State the blood parasite species.
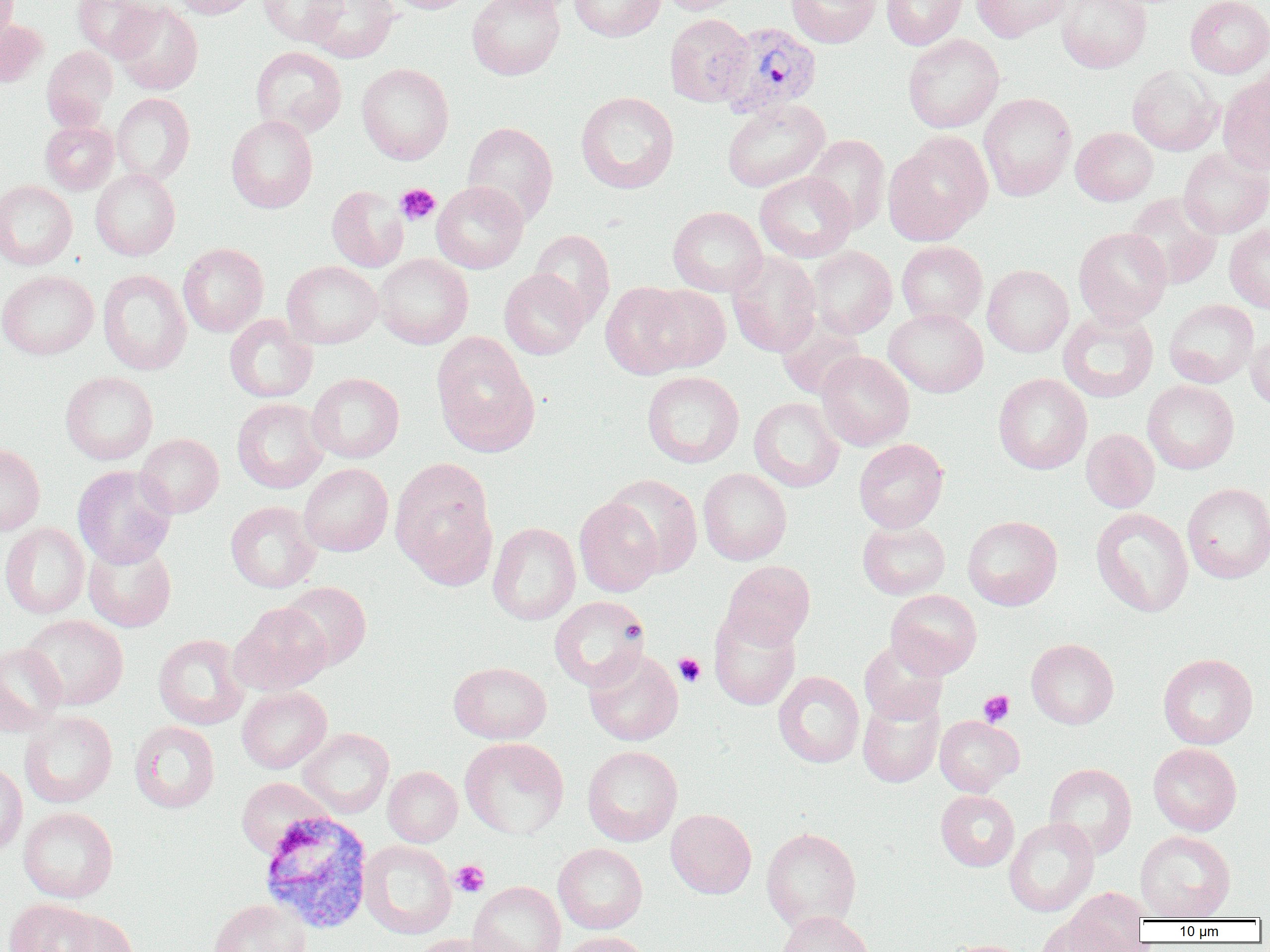

Plasmodium vivax.

Approximate bounding boxes as (x1,y1)-(x2,y2) corner pairs in pixels. Uninfected red blood cell locations: (0,0)-(19,50), (72,0)-(161,60), (168,0)-(258,18), (257,0)-(347,46), (305,0)-(399,62), (386,0)-(478,14), (467,0)-(565,80), (569,0)-(665,41), (659,0)-(747,14), (785,0)-(881,48), (881,0)-(967,50), (886,0)-(977,108), (971,0)-(1070,42), (1056,0)-(1151,73), (1185,0)-(1270,78), (112,1)-(203,95), (664,14)-(754,107), (0,19)-(47,86), (903,33)-(1004,133), (41,46)-(117,131), (250,46)-(347,138), (356,62)-(454,164), (1127,65)-(1221,155), (1218,74)-(1270,175), (576,91)-(679,194), (112,93)-(195,184), (978,93)-(1076,201), (722,98)-(830,192), (226,115)-(318,213), (40,120)-(118,194), (462,121)-(559,226), (1071,127)-(1158,205), (883,132)-(992,246), (804,134)-(890,233), (1178,148)-(1270,238), (91,169)-(180,260), (755,171)-(856,262), (0,181)-(77,270), (431,181)-(529,273), (327,185)-(408,272), (1124,193)-(1223,290), (668,206)-(767,296), (1225,224)-(1270,313), (1073,227)-(1172,327), (529,229)-(615,326), (897,241)-(987,327), (178,243)-(268,336), (807,246)-(897,338), (727,252)-(822,357), (374,254)-(473,349), (282,261)-(383,348), (982,265)-(1074,357), (98,268)-(191,375), (499,268)-(588,359), (0,270)-(98,359), (601,282)-(696,379), (643,284)-(731,373), (1163,299)-(1259,388), (884,308)-(988,397), (1058,309)-(1158,403), (224,314)-(317,403), (776,316)-(866,400), (1246,331)-(1270,411), (432,335)-(540,457), (815,351)-(915,450), (60,371)-(158,465), (642,371)-(744,468), (307,372)-(405,463), (993,373)-(1092,474), (1143,380)-(1239,474), (749,397)-(844,492), (232,398)-(328,493), (1081,428)-(1159,513), (135,433)-(224,518), (854,439)-(948,532), (0,443)-(45,536), (390,458)-(497,584), (298,463)-(393,556), (73,465)-(176,568), (698,468)-(792,565), (605,474)-(703,578), (1182,483)-(1270,583), (574,496)-(664,597), (225,501)-(320,593), (1091,507)-(1194,617), (962,515)-(1062,610), (857,520)-(950,599), (488,522)-(580,625), (0,523)-(89,618), (83,540)-(177,632), (721,560)-(816,648), (279,581)-(371,671), (886,589)-(982,679), (549,596)-(650,691), (229,602)-(332,695), (709,608)-(801,710), (21,614)-(129,710), (153,634)-(249,730), (1026,638)-(1118,729), (859,639)-(948,724), (0,642)-(66,736), (584,649)-(683,746), (1158,653)-(1258,749), (448,661)-(551,744), (773,671)-(864,768), (237,686)-(331,773), (857,692)-(944,788), (19,711)-(117,808), (934,715)-(1024,796), (129,721)-(220,813), (298,728)-(394,818), (459,738)-(569,839), (1148,743)-(1242,835), (582,745)-(682,846), (0,760)-(27,857), (1044,763)-(1137,860), (383,766)-(462,847), (235,777)-(333,859), (935,790)-(1020,871), (18,807)-(118,903), (665,808)-(756,898), (1004,818)-(1099,916), (761,827)-(861,932), (1135,830)-(1236,920), (359,840)-(456,939), (553,843)-(648,934), (468,881)-(565,952), (1063,886)-(1150,951), (4,898)-(99,952), (208,898)-(310,952), (55,909)-(137,952), (776,910)-(874,952), (1037,916)-(1126,951), (559,931)-(651,952), (410,933)-(512,952), (943,939)-(1032,952). Platelet locations: (395,183)-(440,225), (673,653)-(706,687), (979,690)-(1015,727), (451,860)-(490,897). Plasmodium vivax-infected red blood cell locations: (717,21)-(823,119), (258,810)-(375,934). Image is 1270×952 pixels. Thin blood smear. Light microscopy. One field of a larger specimen. 1000x magnification.